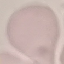

Summary:
  - Result: no malaria parasites seen
  - Stain: Giemsa
  - Image type: cell patch, automatically extracted from a larger field of view and resized to 64 × 64 pixels
  - Capture: smartphone through the microscope eyepiece
  - Preparation: thin smear